Comment on the morphology of the red blood cells.
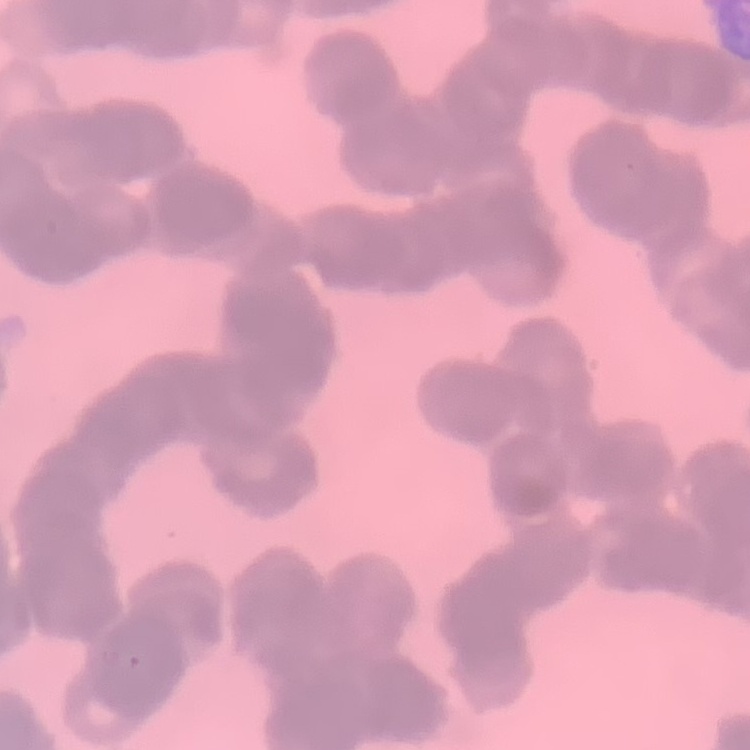

Rouleaux formation.

stain = Field's or Giemsa
preparation = thin peripheral smear
image type = one tile cut from a larger photomicrograph